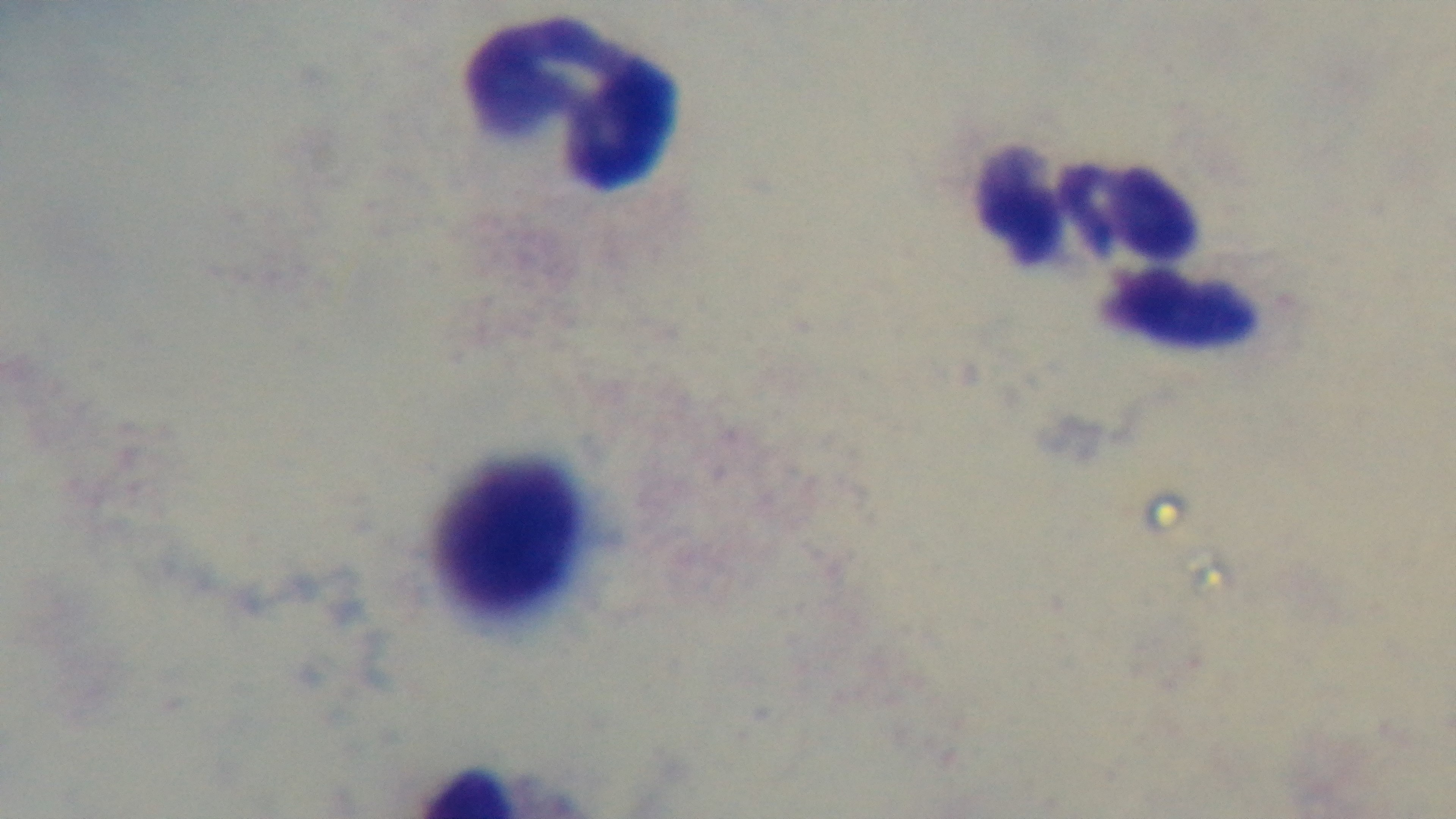
Summary:
  - Field of view: one from the slide
  - Objective: 100x oil immersion
  - Capture: mounted 4K digital camera
  - Stain: Giemsa
  - Malaria status: uninfected
  - Modality: light microscopy
  - Preparation: thick